Report the malaria status of this cell.
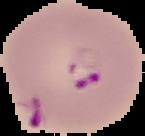

Parasitized.

Cell region segmented out of the field of view; the surrounding area is masked to black. From a thin blood film. Image is 145×136 pixels.